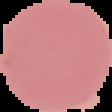 Segmented cell region on a black background. Image is 112×112 pixels. Malaria status: uninfected. From a thin blood film.